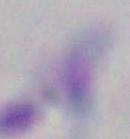

Toxoplasma gondii is shown. Photomicrograph. 1000x magnification.